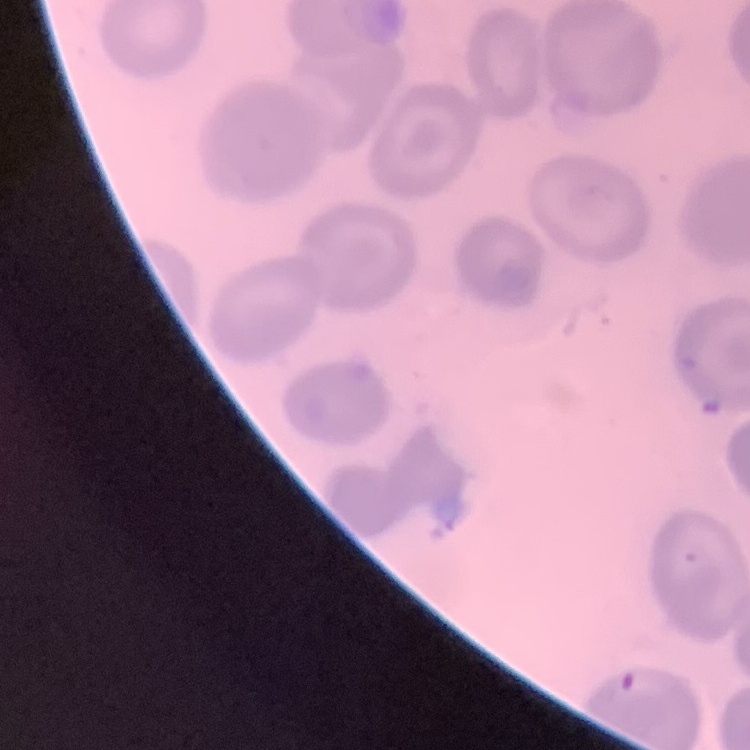

The erythrocytes exhibit no rouleaux formation. Field's or Giemsa stain. Thin peripheral smear. Square crop of a larger photomicrograph.